Classify this cell by malaria status.
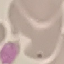
It is uninfected.

Cell patch, automatically extracted from a larger field of view and resized to 64 × 64 pixels. Acquired by smartphone through the microscope eyepiece. Thin smear of blood. Giemsa stain.